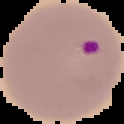
Malaria status: parasitized. Image is 124×124 pixels. From a thin blood film. Segmented cell region on a black background.